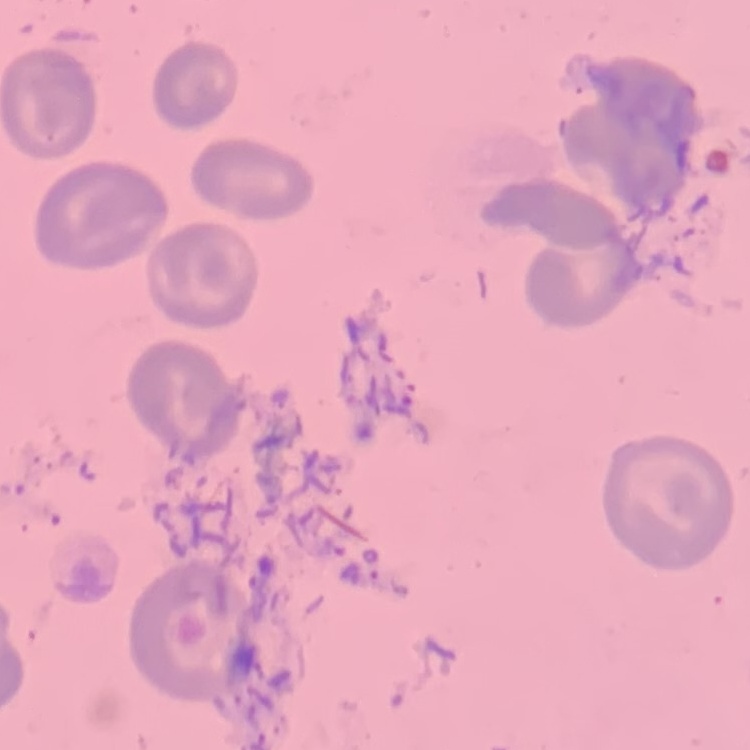
red_blood_cell_morphology: no rouleaux formation
image_type: one tile cut from a larger photomicrograph
preparation: thin peripheral smear
stain: Field's or Giemsa